Name the parasite shown.
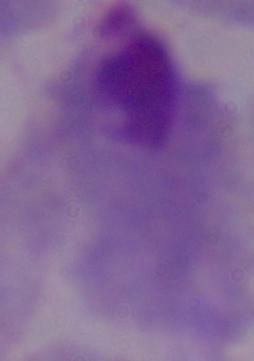

A trichomonad.

Summary:
  - Magnification: 1000x
  - Modality: photomicrograph